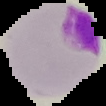 Image is 106×106 pixels. Result: Plasmodium parasites detected. The area outside the segmented cell region is set to black. From a thin blood smear.